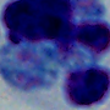
Summary:
  - Modality: micrograph
  - Magnification: 1000x
  - Identification: leukocyte